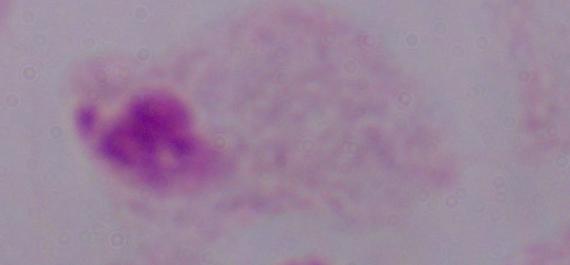
Summary:
  - Modality: micrograph
  - Magnification: 1000x
  - Identification: trichomonad